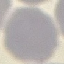

malaria_status: uninfected
capture: smartphone camera at the microscope eyepiece
stain: Giemsa
preparation: thin blood film
image_type: automatically extracted cell patch, resized to 64 × 64 pixels